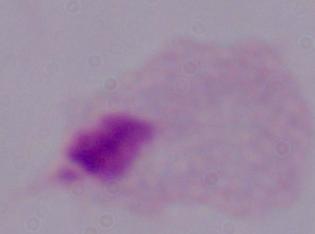
Summary:
  - Modality: photomicrograph
  - Identification: trichomonad
  - Magnification: 1000x